State the preparation type.
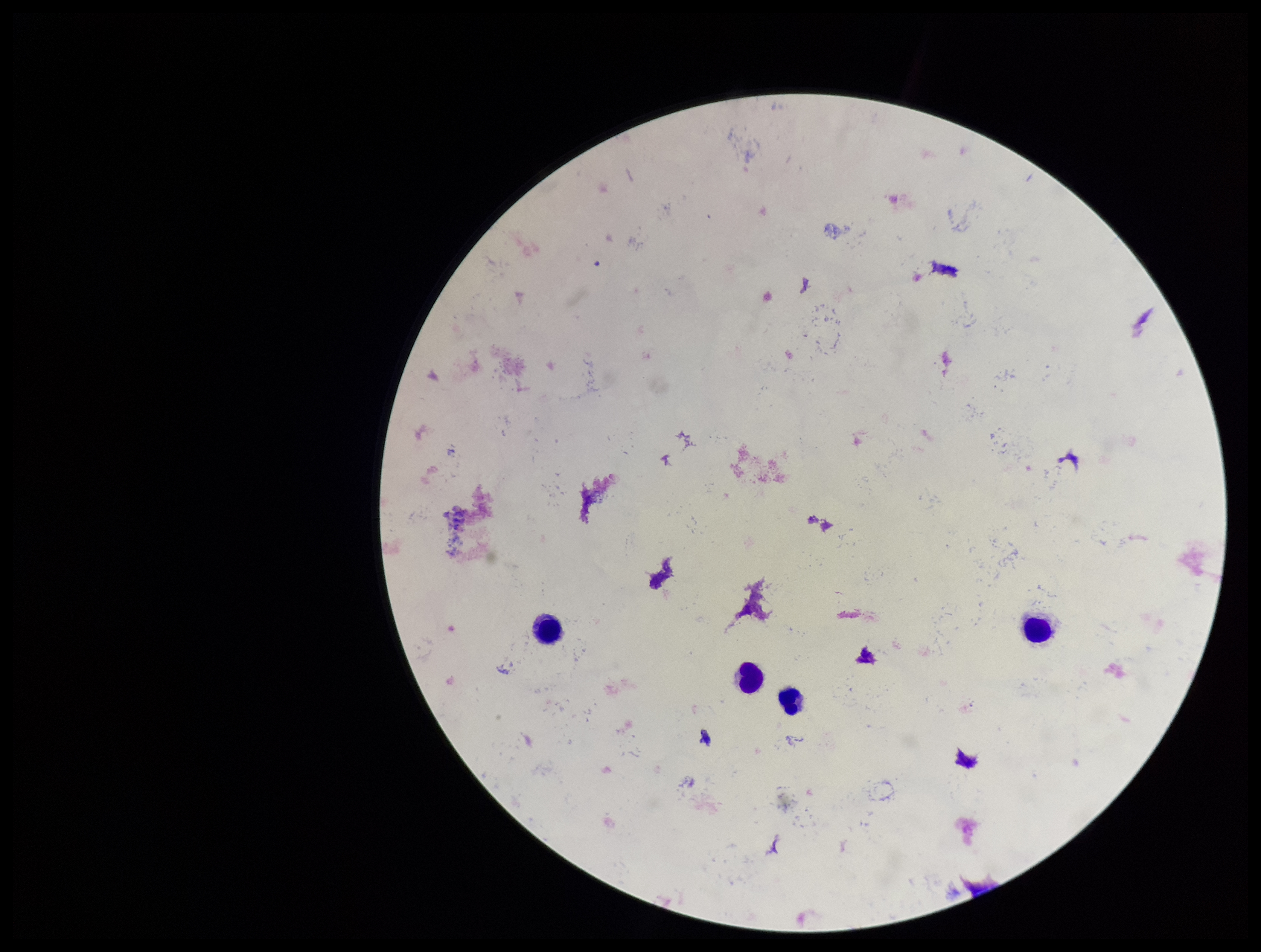

Thick.

Stained with Giemsa. Image is 1261×952 pixels. Plasmodium parasites: none identified. Parasite count: 0. Smartphone photograph taken through the eyepiece of a microscope. Patient malaria status: negative. Leukocyte count: 4. One field from this slide.